Locate every blood parasite and identify its species.
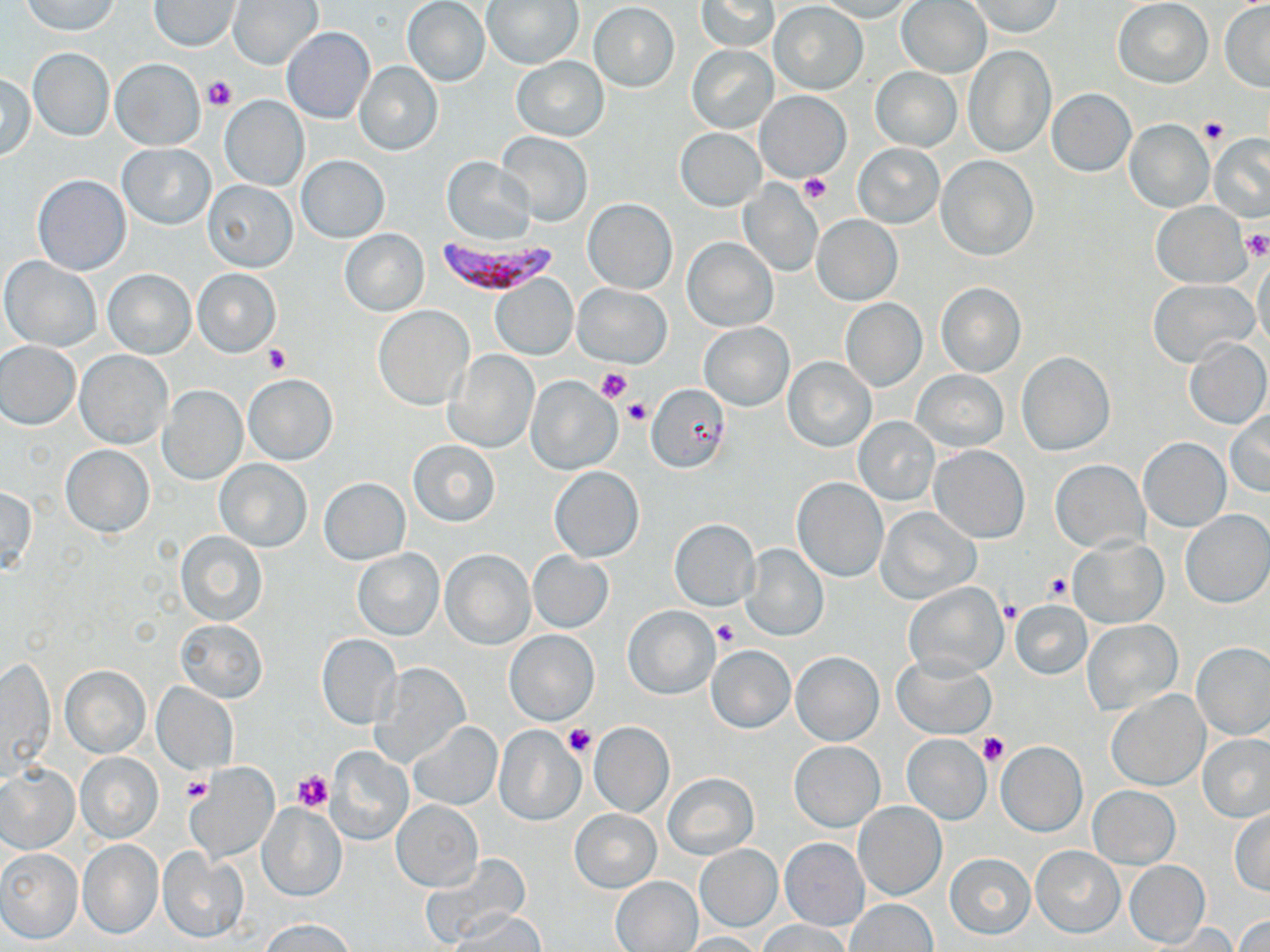

Approximate bounding boxes as [x1, y1, x2, y2] in pixels.
Plasmodium falciparum-infected red blood cells: [434, 236, 560, 296].
No Plasmodium ovale, Plasmodium malariae, Plasmodium vivax, Babesia divergens, or Trypanosoma brucei observed.

slide_level_diagnosis: Plasmodium falciparum
image_size: 1270×952 pixels
field_of_view: single
platelet_locations: 'approximate bounding boxes as [x1, y1, x2, y2] in pixels: [203, 76, 236, 108], [1199, 117, 1229, 143], [798, 172, 830, 204], [1240, 230, 1270, 261], [263, 345, 291, 374], [596, 366, 632, 403], [624, 399, 651, 426], [1043, 572, 1075, 604], [999, 600, 1022, 623], [714, 618, 739, 647], [564, 725, 596, 757], [979, 733, 1009, 765], [293, 769, 333, 811], [182, 776, 212, 804]'
preparation: thin blood film
modality: light microscopy
stain: May-Grünwald-Giemsa
magnification: 1000x
uninfected_red_blood_cell_locations: 'approximate bounding boxes as [x1, y1, x2, y2] in pixels: [149, 0, 241, 50], [228, 0, 323, 69], [695, 0, 777, 52], [814, 0, 919, 22], [1113, 0, 1213, 87], [402, 1, 491, 87], [482, 1, 583, 70], [897, 1, 990, 78], [966, 1, 1063, 37], [21, 2, 122, 37], [1220, 2, 1270, 92], [589, 3, 679, 91], [769, 3, 869, 94], [281, 26, 375, 124], [687, 45, 778, 133], [963, 46, 1055, 157], [27, 48, 114, 141], [511, 57, 608, 140], [110, 58, 205, 150], [354, 60, 442, 155], [870, 67, 962, 152], [1, 73, 36, 161], [1046, 88, 1136, 176], [756, 90, 850, 182], [218, 96, 309, 192], [1124, 119, 1213, 212], [676, 128, 766, 211], [496, 130, 592, 226], [1210, 134, 1270, 223], [853, 143, 943, 228], [118, 144, 215, 229], [297, 155, 389, 242], [442, 156, 536, 245], [937, 156, 1038, 261], [33, 175, 130, 275], [201, 178, 298, 272], [737, 179, 823, 277], [583, 198, 677, 294], [1151, 201, 1250, 287], [811, 214, 903, 306], [340, 229, 428, 316], [683, 237, 777, 331], [1252, 253, 1270, 355], [1, 257, 102, 351], [192, 269, 280, 357], [103, 270, 194, 358], [490, 273, 578, 360], [1147, 278, 1258, 368], [935, 282, 1026, 377], [572, 283, 673, 368], [839, 299, 926, 391], [374, 305, 473, 409], [700, 322, 793, 411], [1182, 337, 1269, 430], [0, 341, 81, 429], [445, 349, 539, 453], [74, 351, 173, 450], [1017, 351, 1115, 455], [783, 356, 877, 452], [912, 370, 1008, 451], [243, 373, 337, 466], [526, 376, 621, 473], [159, 385, 247, 484], [645, 385, 732, 472], [1226, 408, 1270, 497], [852, 417, 939, 506], [1139, 437, 1229, 531], [408, 439, 500, 526], [61, 444, 154, 537], [929, 445, 1029, 543], [215, 459, 312, 551], [1051, 461, 1148, 552], [550, 466, 644, 562], [791, 477, 888, 582], [319, 478, 410, 564], [0, 486, 37, 572], [877, 508, 981, 605], [1180, 510, 1270, 607], [669, 519, 760, 612], [175, 529, 268, 627], [1069, 537, 1167, 628], [740, 542, 829, 641], [353, 548, 445, 639], [441, 549, 534, 649], [527, 551, 615, 633], [903, 582, 1007, 678], [1010, 600, 1091, 679], [623, 607, 719, 699], [175, 619, 268, 704], [1083, 620, 1182, 714], [504, 629, 599, 726], [316, 633, 401, 729], [1191, 642, 1270, 740], [706, 644, 795, 733], [791, 652, 883, 745], [2, 654, 55, 782], [893, 656, 996, 739], [374, 661, 470, 769], [60, 665, 150, 757], [152, 682, 238, 774], [1106, 689, 1209, 790], [408, 721, 502, 810], [589, 721, 674, 818], [493, 725, 585, 826], [900, 734, 993, 825], [1198, 734, 1270, 823], [790, 741, 884, 831], [995, 741, 1087, 836], [325, 745, 412, 846], [76, 753, 163, 843], [0, 762, 79, 854], [186, 763, 279, 864], [662, 771, 758, 861], [1087, 786, 1181, 868], [392, 801, 483, 890], [854, 801, 946, 900], [258, 803, 348, 901], [1230, 809, 1270, 895], [570, 810, 660, 892], [779, 837, 870, 931], [77, 840, 164, 940], [695, 845, 782, 931], [1030, 845, 1125, 938], [158, 848, 249, 943], [0, 849, 82, 944], [422, 852, 528, 946], [945, 852, 1035, 939], [1123, 859, 1210, 947], [612, 877, 702, 951], [844, 899, 938, 952], [456, 910, 546, 950], [1236, 914, 1270, 951], [260, 918, 358, 952], [760, 920, 850, 952], [1148, 925, 1239, 952], [679, 932, 764, 951]'